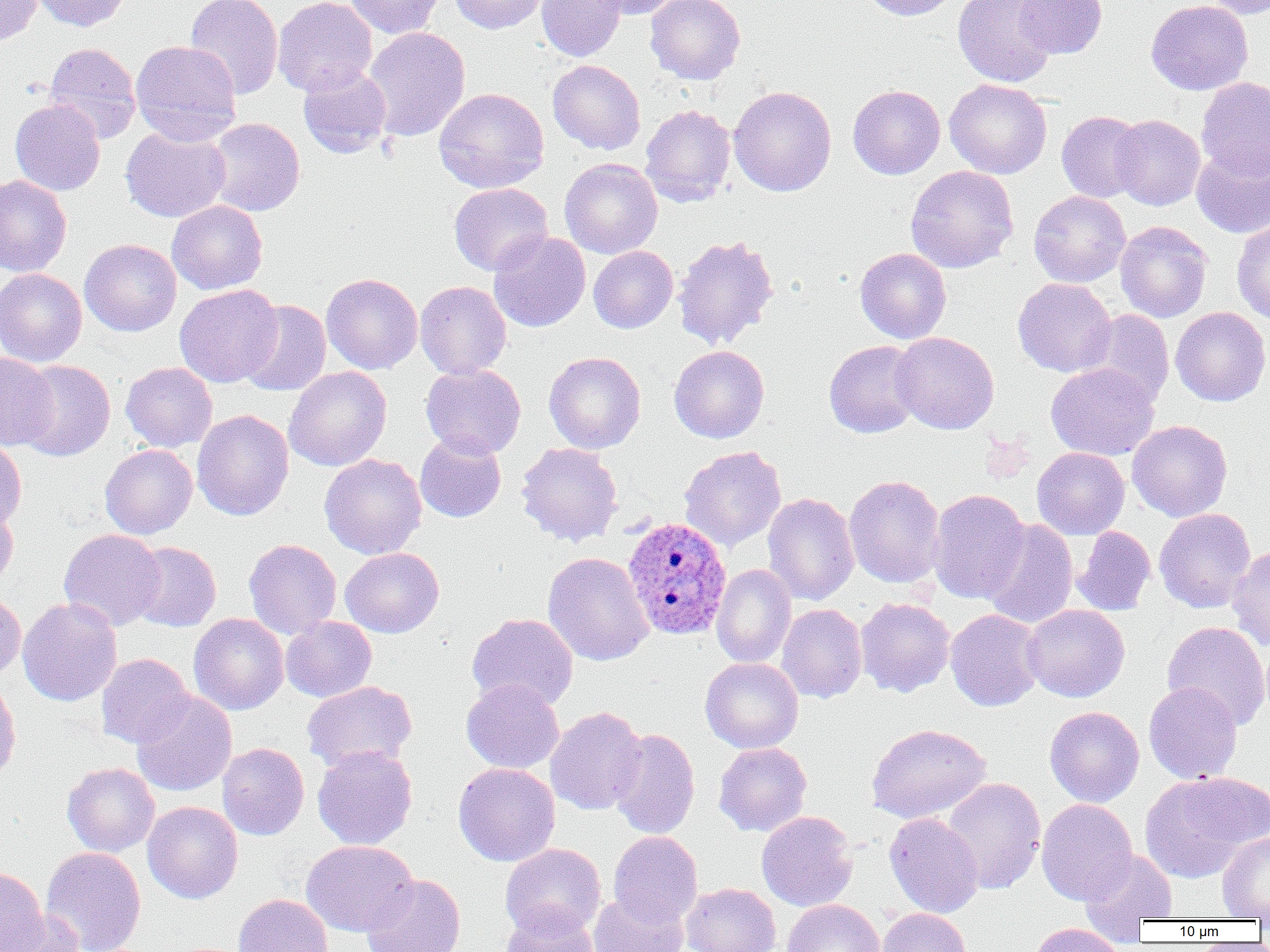

Summary:
  - Coordinate format: approximate bounding boxes as named x1/y1/x2/y2 corners in pixels
  - Plasmodium ovale-infected red blood cell locations: (x1=622, y1=516, x2=733, y2=641)
  - Uninfected red blood cell locations: (x1=0, y1=0, x2=43, y2=46), (x1=33, y1=0, x2=132, y2=31), (x1=185, y1=0, x2=283, y2=100), (x1=273, y1=0, x2=377, y2=96), (x1=344, y1=0, x2=444, y2=39), (x1=448, y1=0, x2=550, y2=34), (x1=536, y1=0, x2=627, y2=62), (x1=590, y1=0, x2=687, y2=19), (x1=646, y1=0, x2=745, y2=84), (x1=860, y1=0, x2=960, y2=20), (x1=953, y1=0, x2=1059, y2=88), (x1=1014, y1=0, x2=1108, y2=59), (x1=1146, y1=0, x2=1253, y2=95), (x1=1200, y1=0, x2=1270, y2=19), (x1=362, y1=27, x2=471, y2=141), (x1=130, y1=40, x2=242, y2=146), (x1=44, y1=42, x2=141, y2=143), (x1=547, y1=59, x2=646, y2=154), (x1=298, y1=65, x2=392, y2=159), (x1=1196, y1=77, x2=1270, y2=179), (x1=944, y1=78, x2=1052, y2=179), (x1=847, y1=85, x2=945, y2=179), (x1=728, y1=86, x2=837, y2=197), (x1=433, y1=87, x2=549, y2=193), (x1=10, y1=99, x2=106, y2=196), (x1=640, y1=105, x2=736, y2=207), (x1=1057, y1=111, x2=1146, y2=203), (x1=1110, y1=115, x2=1205, y2=210), (x1=205, y1=118, x2=305, y2=217), (x1=120, y1=126, x2=231, y2=223), (x1=1191, y1=143, x2=1270, y2=238), (x1=560, y1=158, x2=662, y2=259), (x1=905, y1=165, x2=1019, y2=273), (x1=0, y1=174, x2=72, y2=277), (x1=448, y1=183, x2=553, y2=276), (x1=1028, y1=190, x2=1130, y2=287), (x1=167, y1=200, x2=268, y2=295), (x1=1232, y1=218, x2=1270, y2=325), (x1=1115, y1=221, x2=1212, y2=323), (x1=488, y1=230, x2=591, y2=332), (x1=673, y1=234, x2=779, y2=351), (x1=79, y1=238, x2=182, y2=337), (x1=588, y1=246, x2=678, y2=333), (x1=854, y1=247, x2=951, y2=344), (x1=0, y1=267, x2=88, y2=367), (x1=321, y1=273, x2=423, y2=374), (x1=1013, y1=278, x2=1117, y2=378), (x1=415, y1=280, x2=512, y2=379), (x1=174, y1=284, x2=283, y2=387), (x1=238, y1=300, x2=332, y2=396), (x1=1170, y1=306, x2=1270, y2=407), (x1=1082, y1=310, x2=1174, y2=409), (x1=891, y1=332, x2=999, y2=434), (x1=823, y1=340, x2=924, y2=438), (x1=669, y1=345, x2=769, y2=443), (x1=544, y1=351, x2=646, y2=454), (x1=0, y1=353, x2=59, y2=451), (x1=16, y1=360, x2=115, y2=461), (x1=120, y1=362, x2=217, y2=452), (x1=1046, y1=362, x2=1159, y2=461), (x1=420, y1=363, x2=526, y2=459), (x1=283, y1=366, x2=392, y2=472), (x1=192, y1=410, x2=294, y2=521), (x1=1127, y1=420, x2=1233, y2=522), (x1=415, y1=433, x2=506, y2=522), (x1=0, y1=439, x2=26, y2=532), (x1=516, y1=442, x2=623, y2=546), (x1=100, y1=444, x2=197, y2=539), (x1=679, y1=446, x2=786, y2=552), (x1=1031, y1=447, x2=1130, y2=540), (x1=319, y1=454, x2=426, y2=559), (x1=844, y1=474, x2=946, y2=588), (x1=928, y1=488, x2=1030, y2=604), (x1=762, y1=492, x2=860, y2=606), (x1=0, y1=503, x2=18, y2=593), (x1=1154, y1=508, x2=1256, y2=613), (x1=981, y1=519, x2=1079, y2=630), (x1=1073, y1=526, x2=1156, y2=615), (x1=58, y1=528, x2=166, y2=631), (x1=243, y1=539, x2=342, y2=639), (x1=129, y1=542, x2=221, y2=631), (x1=1227, y1=543, x2=1270, y2=651), (x1=340, y1=547, x2=444, y2=637), (x1=543, y1=552, x2=654, y2=666), (x1=712, y1=564, x2=796, y2=668), (x1=0, y1=589, x2=26, y2=682), (x1=17, y1=597, x2=122, y2=706), (x1=855, y1=597, x2=955, y2=697), (x1=776, y1=603, x2=867, y2=703), (x1=1022, y1=604, x2=1130, y2=702), (x1=945, y1=608, x2=1045, y2=712), (x1=466, y1=612, x2=578, y2=711), (x1=189, y1=613, x2=289, y2=715), (x1=280, y1=616, x2=377, y2=702), (x1=1162, y1=621, x2=1270, y2=731), (x1=96, y1=653, x2=194, y2=748), (x1=701, y1=657, x2=804, y2=753), (x1=0, y1=677, x2=21, y2=788), (x1=461, y1=678, x2=564, y2=774), (x1=302, y1=680, x2=418, y2=772), (x1=1143, y1=681, x2=1243, y2=784), (x1=132, y1=691, x2=236, y2=797), (x1=545, y1=706, x2=648, y2=815), (x1=1044, y1=706, x2=1144, y2=807), (x1=866, y1=723, x2=991, y2=823), (x1=608, y1=728, x2=700, y2=840), (x1=217, y1=742, x2=309, y2=840), (x1=713, y1=742, x2=812, y2=836), (x1=312, y1=745, x2=418, y2=850), (x1=62, y1=762, x2=160, y2=856), (x1=453, y1=762, x2=560, y2=866), (x1=1186, y1=772, x2=1270, y2=849), (x1=1139, y1=773, x2=1259, y2=883), (x1=942, y1=777, x2=1045, y2=894), (x1=1036, y1=798, x2=1138, y2=904), (x1=142, y1=801, x2=243, y2=904), (x1=757, y1=810, x2=858, y2=912), (x1=884, y1=812, x2=984, y2=918), (x1=1217, y1=830, x2=1270, y2=920), (x1=608, y1=831, x2=702, y2=927), (x1=301, y1=840, x2=419, y2=936), (x1=500, y1=843, x2=606, y2=939), (x1=40, y1=846, x2=146, y2=952), (x1=1078, y1=847, x2=1178, y2=931), (x1=0, y1=866, x2=48, y2=952), (x1=360, y1=874, x2=466, y2=952), (x1=681, y1=882, x2=781, y2=952), (x1=587, y1=891, x2=689, y2=952), (x1=234, y1=894, x2=333, y2=952), (x1=783, y1=899, x2=884, y2=952), (x1=500, y1=906, x2=599, y2=952), (x1=877, y1=908, x2=971, y2=952), (x1=3, y1=911, x2=86, y2=952), (x1=1028, y1=922, x2=1127, y2=952)
  - Slide-level diagnosis: Plasmodium ovale
  - Magnification: 1000x
  - Image size: 1270×952 pixels
  - Modality: optical microscopy
  - Preparation: thin blood smear
  - Field of view: one of a larger specimen